State which cell type is depicted.
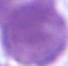
This is an erythrocyte.

{
  "magnification": "1000x",
  "modality": "photomicrograph"
}